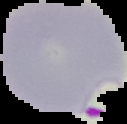

Summary:
  - Image type: segmented cell region on a black background
  - Preparation: thin blood smear
  - Image size: 127×124 pixels
  - Malaria status: parasitized